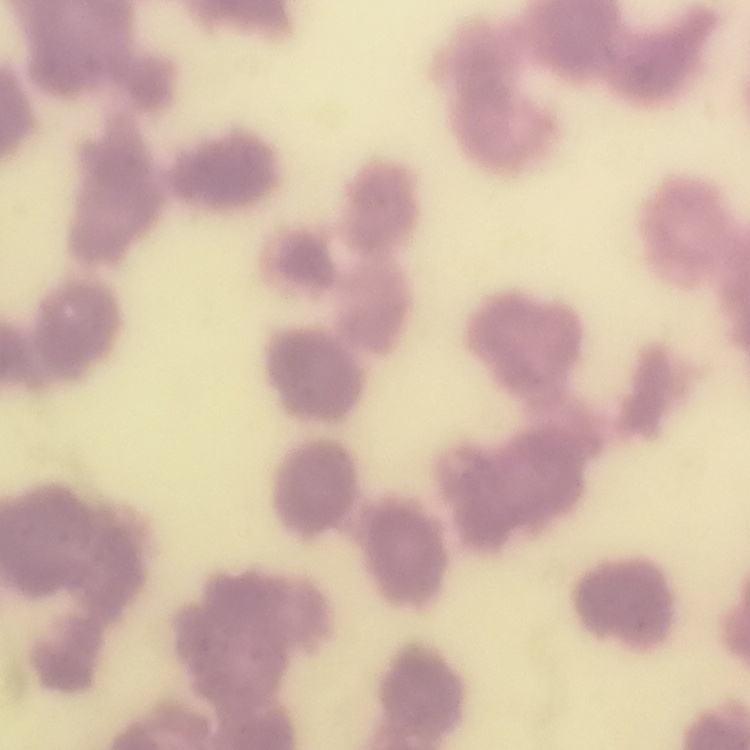
The erythrocytes show rouleaux formation. One tile cut from a larger photomicrograph. Field's or Giemsa stain. Thin peripheral smear.